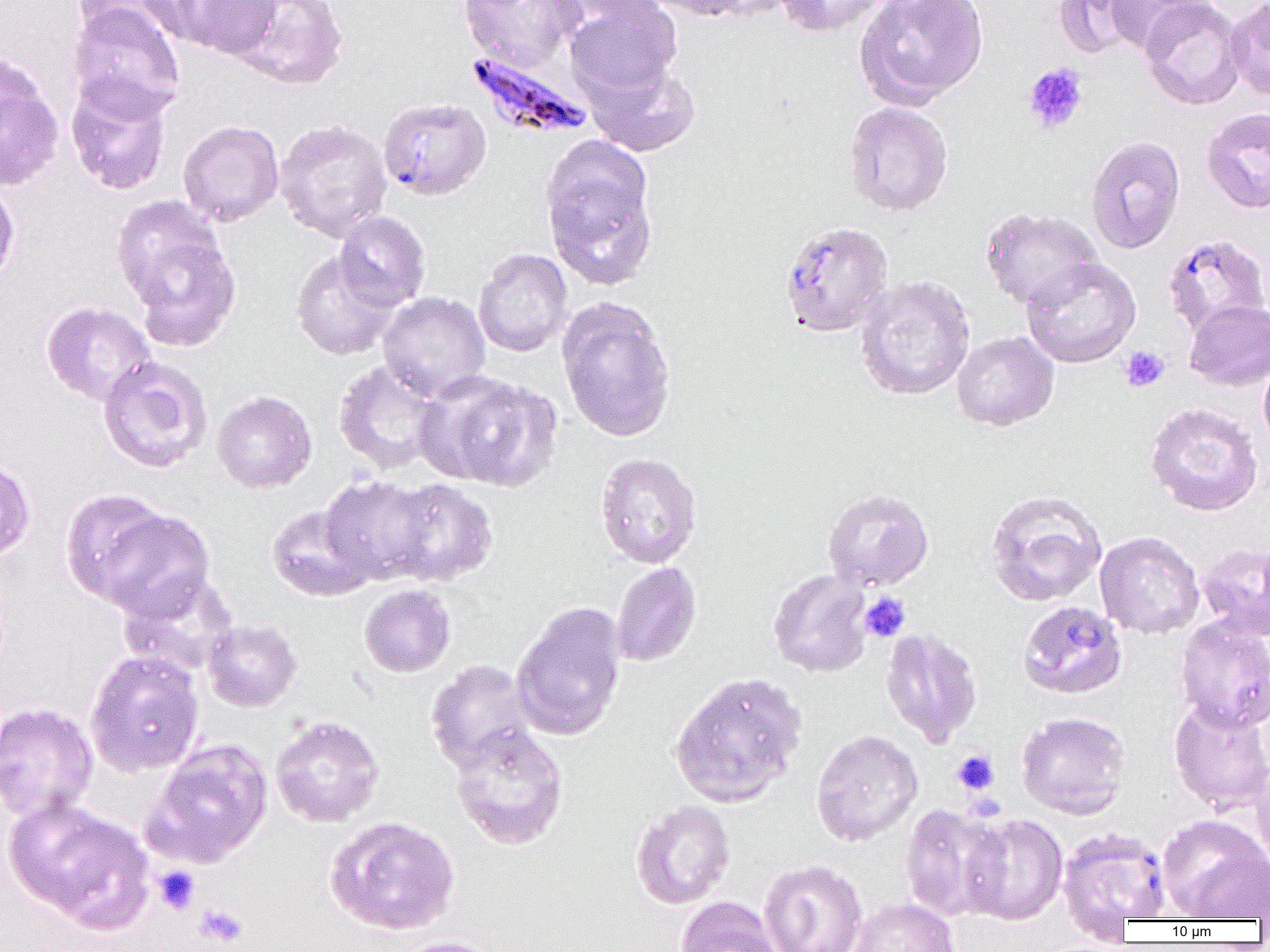
slide-level diagnosis = Plasmodium falciparum
modality = optical microscopy
image size = 1270×952 pixels
magnification = 1000x
preparation = thin blood smear
platelet locations = approximate bounding boxes as (x1,y1)-(x2,y2) corner pairs in pixels: (1022,62)-(1089,134), (1120,346)-(1170,392), (859,592)-(911,642), (951,749)-(1000,795), (153,866)-(201,915), (195,903)-(249,948)
Plasmodium falciparum-infected red blood cell locations = approximate bounding boxes as (x1,y1)-(x2,y2) corner pairs in pixels: (465,51)-(594,141), (377,97)-(492,201), (1162,233)-(1269,339), (1017,600)-(1127,699), (1058,827)-(1172,925)
field of view = one of a larger specimen
uninfected red blood cell locations = approximate bounding boxes as (x1,y1)-(x2,y2) corner pairs in pixels: (71,0)-(177,44), (164,0)-(283,59), (226,0)-(349,91), (459,0)-(584,70), (549,0)-(669,32), (643,0)-(768,21), (773,0)-(889,37), (854,0)-(989,110), (1052,0)-(1151,59), (1103,0)-(1214,55), (1139,0)-(1247,110), (1225,0)-(1270,101), (565,1)-(682,101), (67,3)-(186,119), (0,58)-(65,193), (584,58)-(701,157), (65,75)-(174,195), (844,102)-(953,216), (1200,108)-(1270,213), (273,118)-(392,242), (177,120)-(284,227), (539,135)-(660,290), (1085,135)-(1186,254), (0,181)-(20,294), (979,207)-(1104,313), (333,211)-(431,312), (119,213)-(241,349), (779,221)-(894,338), (473,248)-(573,357), (290,250)-(400,360), (1021,258)-(1141,368), (854,274)-(976,400), (377,291)-(491,401), (556,297)-(678,443), (1184,299)-(1270,391), (40,300)-(157,406), (951,331)-(1059,431), (1258,353)-(1270,453), (97,357)-(214,474), (333,360)-(448,475), (421,371)-(562,491), (212,390)-(317,494), (1145,402)-(1264,516), (594,452)-(702,568), (0,458)-(36,562), (320,474)-(438,584), (379,478)-(499,587), (60,488)-(178,609), (822,488)-(933,590), (985,490)-(1107,607), (266,504)-(377,601), (93,507)-(216,621), (1094,531)-(1205,639), (1197,542)-(1270,641), (610,561)-(702,667), (768,568)-(873,677), (120,573)-(240,677), (359,584)-(456,677), (511,601)-(627,742), (1175,614)-(1270,731), (203,619)-(302,711), (879,627)-(983,747), (84,650)-(205,776), (425,659)-(538,775), (669,671)-(807,808), (1167,696)-(1270,814), (0,702)-(99,823), (1016,711)-(1131,819), (270,716)-(385,828), (450,724)-(569,850), (811,729)-(923,846), (144,740)-(273,868), (1249,757)-(1270,871), (6,799)-(154,932), (630,799)-(736,909), (900,803)-(1006,921), (959,813)-(1068,925), (324,815)-(460,936), (1158,815)-(1269,920), (759,859)-(867,952), (675,896)-(782,952), (848,897)-(960,952), (389,936)-(500,952)